Identify the parasite.
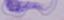

A trypanosome.

Summary:
  - Magnification: 1000x
  - Modality: photomicrograph